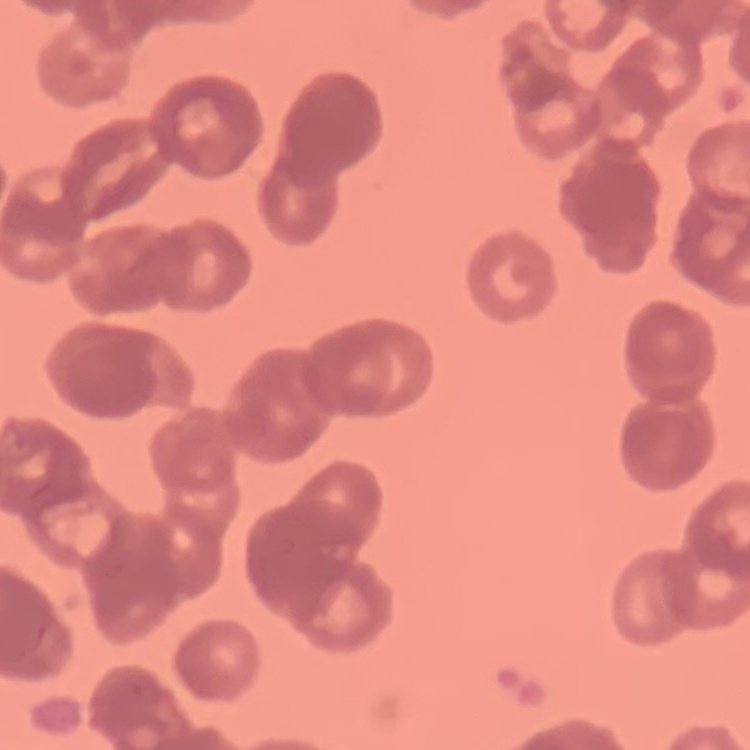
The red blood cells exhibit rouleaux formation. One tile cut from a larger photomicrograph. Thin blood film. Field's or Giemsa stain.